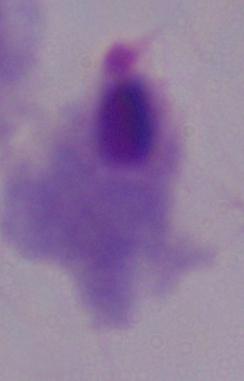
Captured at 1000x magnification. Micrograph. A trichomonad is seen.